Outline each P. falciparum parasite and classify it by life-cycle stage.
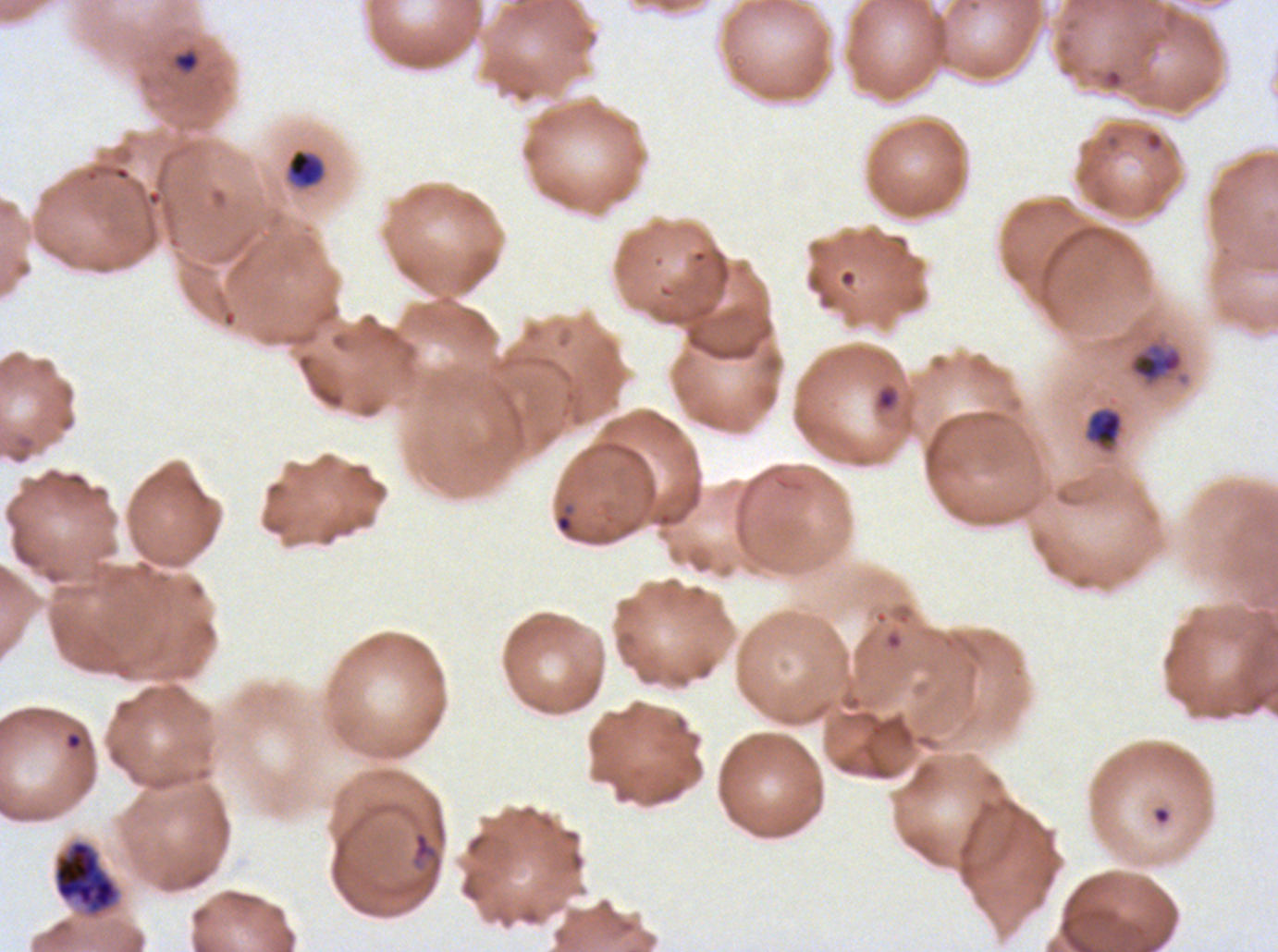
Approximate bounding boxes as {x1, y1, x2, y2} in pixels.
Rings: {1104, 68, 1123, 88}, {876, 387, 898, 410}, {556, 514, 572, 532}, {411, 830, 443, 872}.
Late-ring/early-trophozoite forms: {288, 150, 323, 187}, {1087, 409, 1123, 447}.
Late trophozoites: {1130, 343, 1183, 383}.
Early schizonts: {53, 838, 121, 918}.
No mid trophozoites, late schizonts, segmenters, or gametocytes observed.

A sub-image separated from a larger composite. P. falciparum from a patient in The Gambia, cultured ex vivo for 24 to 48 hours. Image is 1278×952 pixels. Life-cycle stages observed: ring, late-ring/early-trophozoite, late trophozoite, early schizont. Giemsa-stained preparation. Thin blood smear.